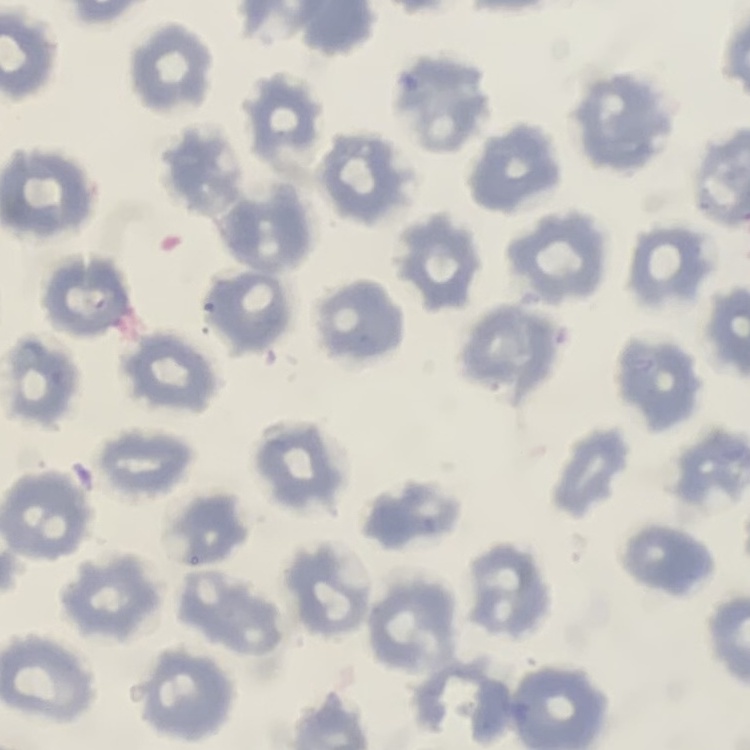
red_blood_cell_morphology: no rouleaux formation
stain: Field's or Giemsa
image_type: square crop of a larger photomicrograph
preparation: thin blood film